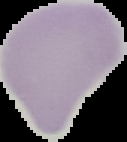 Malaria status: uninfected. Image is 127×142 pixels. From a thin blood smear. Cell region segmented out of the field of view; the surrounding area is masked to black.